Describe the morphology of the red blood cells.
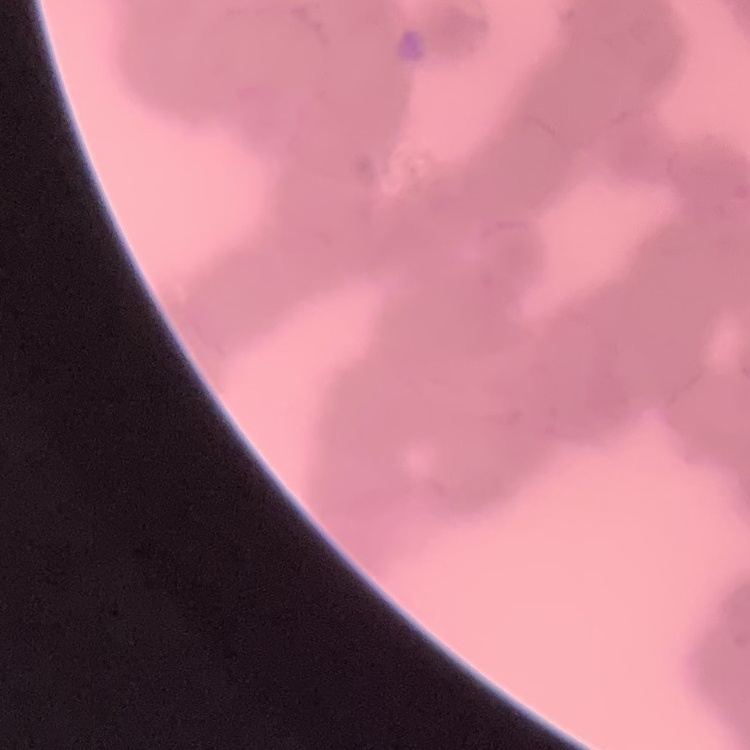
They show rouleaux formation.

preparation = thin blood film
stain = Field's or Giemsa
image type = square crop of a larger photomicrograph